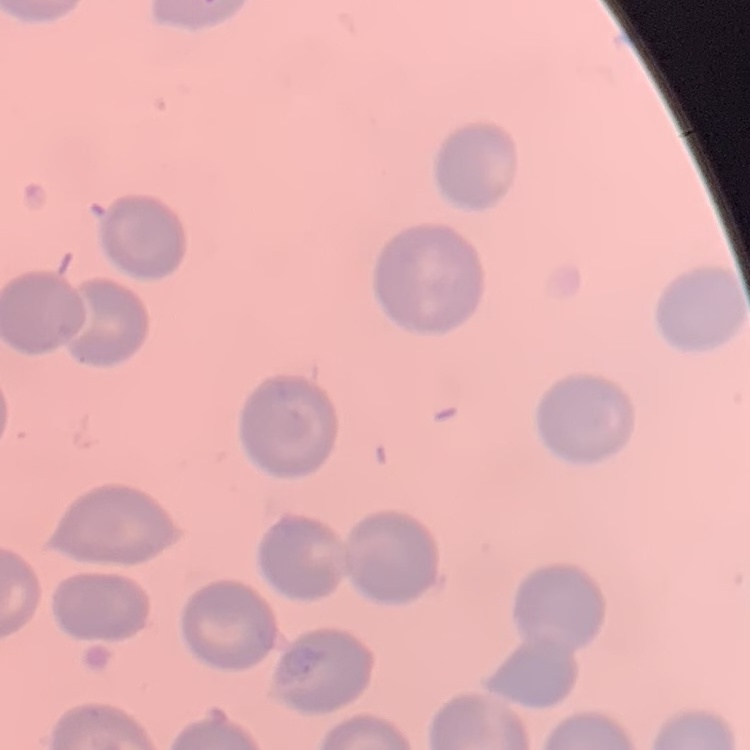

The erythrocytes exhibit no rouleaux formation. Stained with either Field's or Giemsa. Thin blood film. One tile cut from a larger photomicrograph.